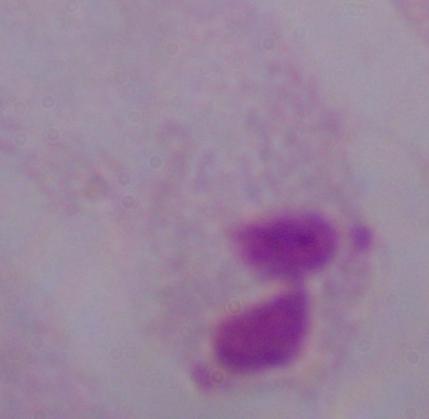 A trichomonad is shown. Captured at 1000x magnification. Micrograph.